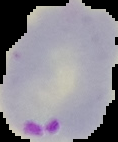

Summary:
  - Image size: 118×142 pixels
  - Malaria status: parasitized
  - Preparation: thin blood smear
  - Image type: segmented cell region on a black background